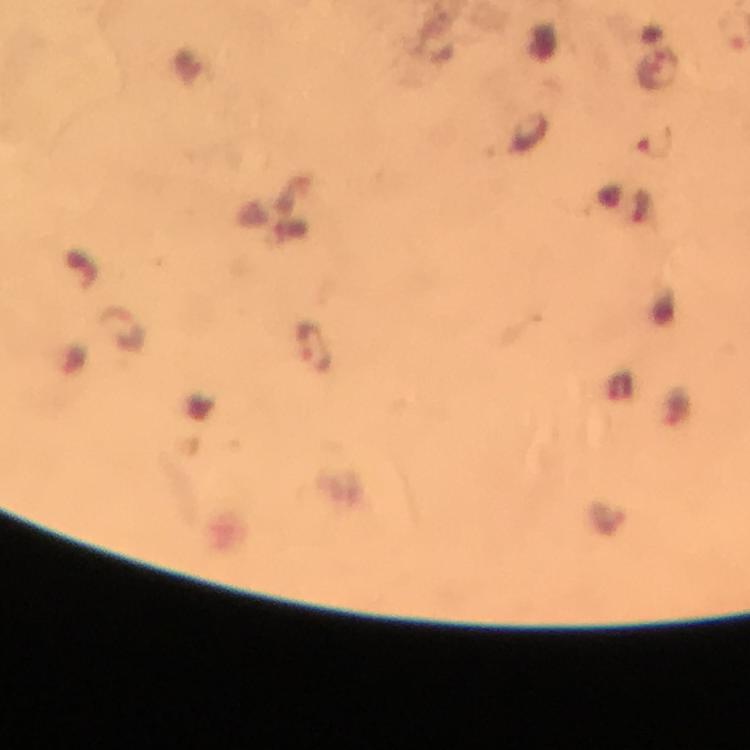

Approximate object centers, in pixels from the top-left corner.
Summary:
  - Plasmodium parasite locations: (x=654, y=144), (x=130, y=328), (x=314, y=348)
  - Magnification: 100x
  - Immersion oil: applied
  - Image size: 750×750 pixels
  - Stain: Giemsa
  - Capture: smartphone photograph through a microscope
  - Cropped from: a single field of view
  - Context: from a malaria diagnostic workup
  - Preparation: thick blood smear